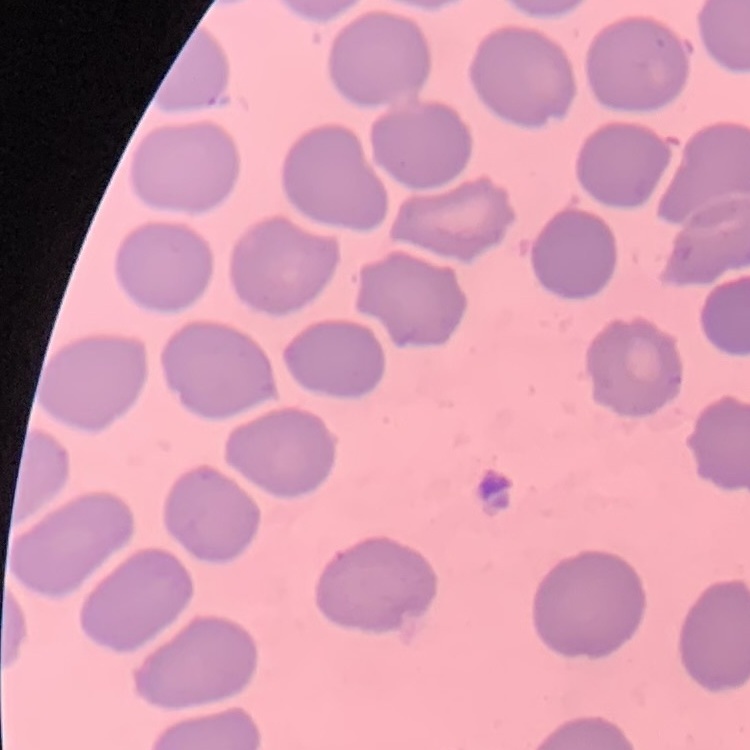

red blood cell morphology = no rouleaux formation
image type = square crop of a larger photomicrograph
stain = Field's or Giemsa
preparation = thin blood smear